Assess this cell for malaria.
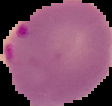
It is parasitized.

preparation: thin blood film
image_type: segmented cell region with the area outside set to black
image_size: 112×106 pixels